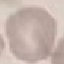
Summary:
  - Malaria status: uninfected
  - Image type: automatically extracted cell patch, resized to 64 × 64 pixels
  - Preparation: thin smear
  - Stain: Giemsa
  - Capture: smartphone through the microscope eyepiece